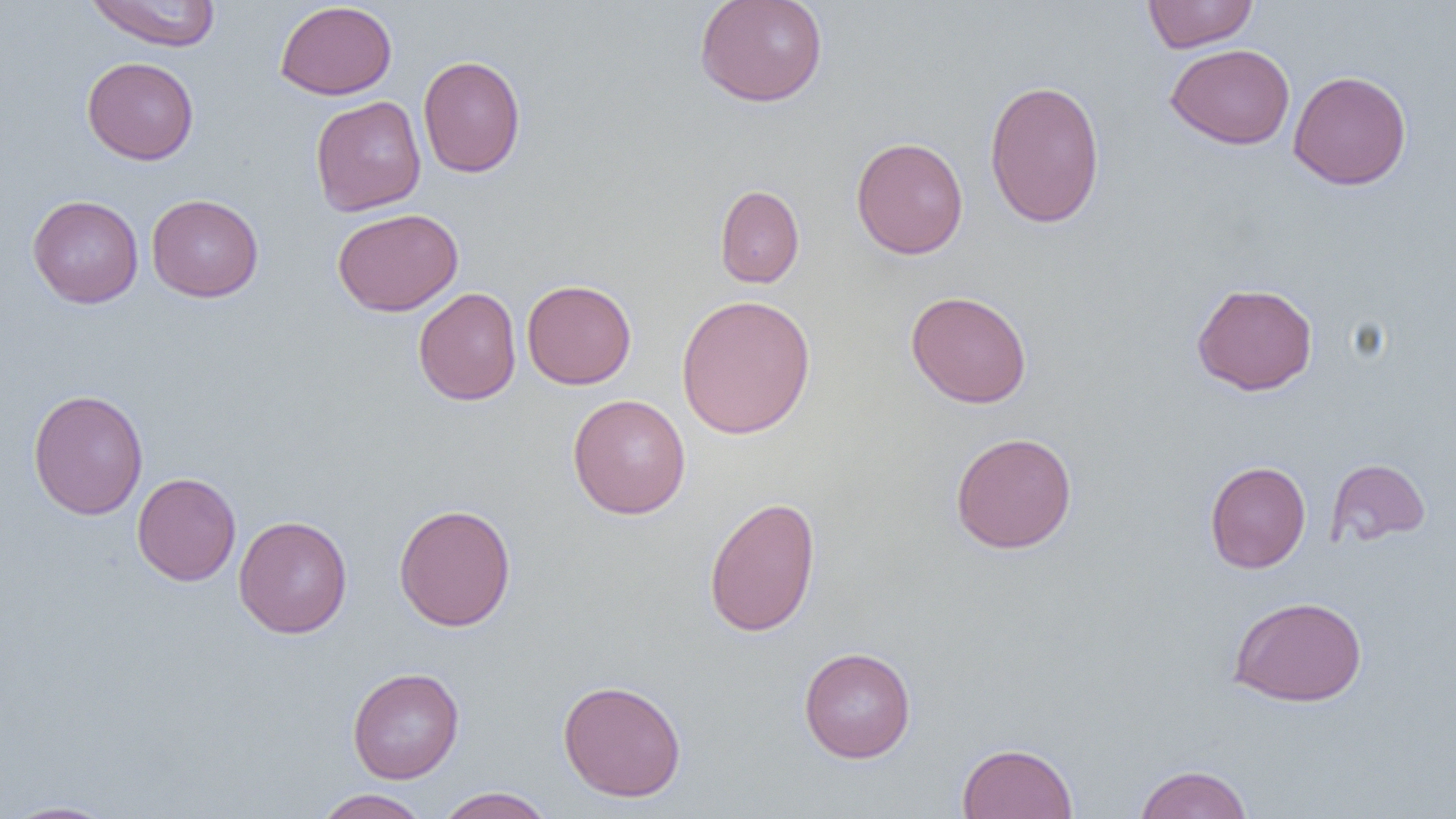
Summary:
  - Coordinate format: approximate bounding boxes as [x1, y1, x2, y2] in pixels
  - Uninfected red blood cell locations: [83, 0, 222, 51], [694, 0, 828, 107], [1142, 0, 1258, 53], [274, 1, 397, 100], [1165, 43, 1295, 149], [418, 55, 526, 178], [82, 56, 199, 165], [1288, 70, 1412, 190], [984, 79, 1105, 228], [310, 96, 426, 215], [850, 136, 968, 259], [714, 184, 805, 288], [146, 193, 263, 302], [27, 194, 144, 308], [332, 208, 463, 316], [522, 279, 637, 389], [1192, 282, 1318, 395], [413, 287, 521, 406], [905, 290, 1032, 408], [675, 294, 816, 440], [28, 388, 148, 520], [567, 394, 691, 519], [949, 432, 1077, 554], [1326, 457, 1430, 547], [1205, 460, 1311, 573], [132, 472, 241, 586], [703, 496, 821, 637], [393, 503, 516, 632], [233, 515, 353, 638], [1228, 595, 1367, 707], [798, 646, 916, 763], [347, 667, 464, 783], [557, 679, 687, 802], [957, 742, 1078, 819], [1133, 764, 1254, 819], [434, 786, 556, 819], [315, 789, 430, 819], [1, 800, 121, 819]
  - Slide-level diagnosis: negative for blood parasites
  - Modality: optical microscopy
  - Magnification: 1000x
  - Field of view: single
  - Preparation: thin blood smear
  - Image size: 1456×819 pixels